Locate every Plasmodium ovale-infected red blood cell.
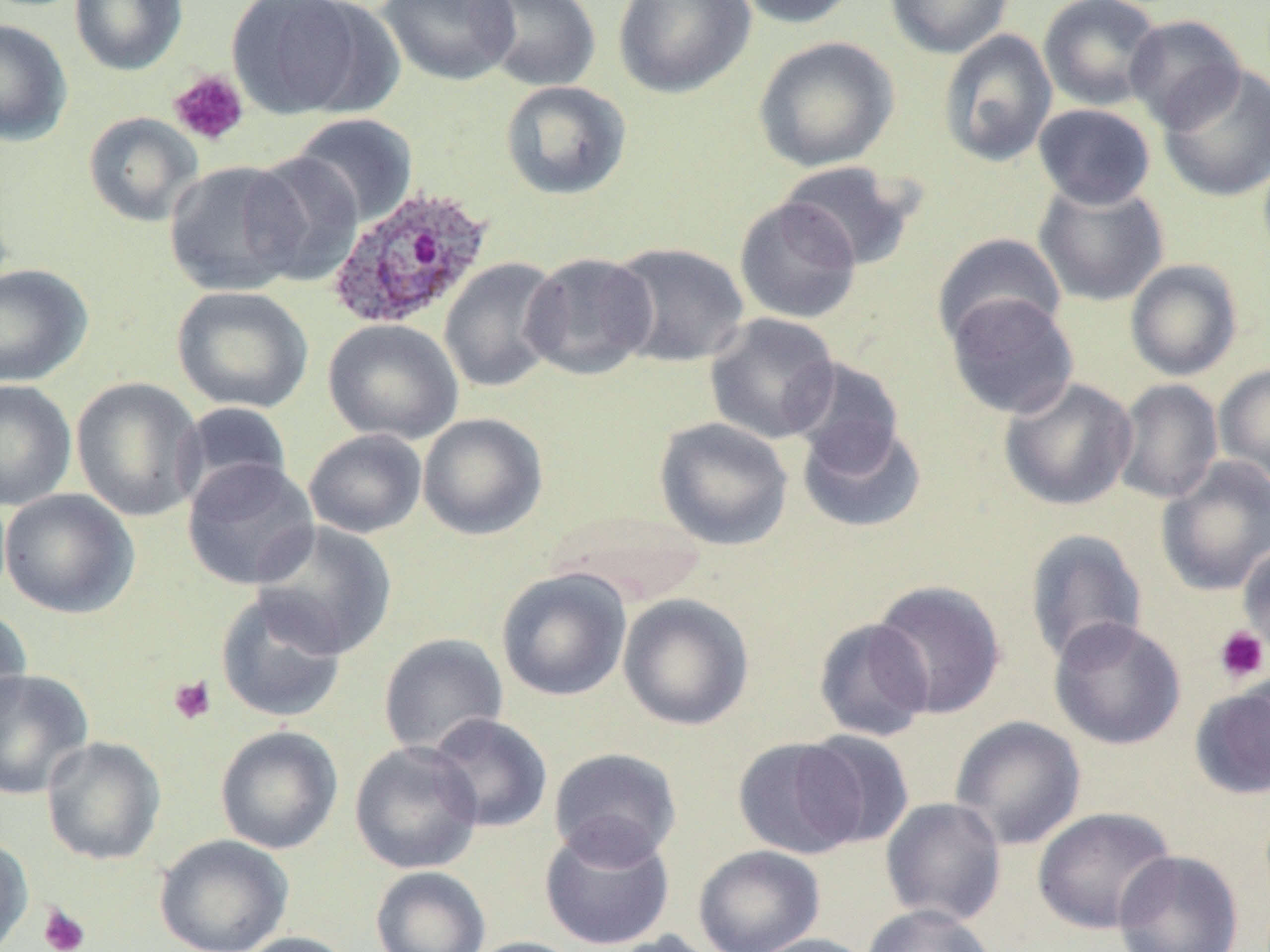
Approximate bounding boxes as (x1,y1)-(x2,y2) corner pairs in pixels.
Plasmodium ovale-infected red blood cells: (326,185)-(493,331).

Summary:
  - Uninfected red blood cell locations: (69,0)-(189,76), (225,0)-(378,119), (377,0)-(519,85), (473,0)-(603,92), (612,0)-(756,99), (731,0)-(862,29), (885,0)-(1014,58), (1038,0)-(1165,111), (1124,14)-(1246,133), (0,18)-(73,146), (937,29)-(1058,168), (752,35)-(900,173), (1157,62)-(1270,202), (500,81)-(632,201), (1033,103)-(1156,209), (82,112)-(203,227), (290,113)-(419,227), (244,152)-(365,286), (163,160)-(308,297), (776,161)-(918,271), (1033,181)-(1169,307), (733,196)-(862,324), (932,232)-(1067,347), (607,241)-(749,368), (521,251)-(658,380), (439,257)-(564,393), (1125,259)-(1243,381), (0,263)-(93,387), (171,285)-(314,414), (945,292)-(1079,419), (704,312)-(841,444), (323,319)-(464,445), (786,357)-(905,473), (1214,363)-(1270,486), (70,377)-(206,521), (998,377)-(1137,511), (0,379)-(77,511), (1113,379)-(1224,505), (173,401)-(294,509), (417,413)-(548,540), (654,417)-(794,550), (797,419)-(928,534), (303,429)-(427,538), (1155,455)-(1270,597), (181,457)-(320,591), (0,488)-(139,618), (547,509)-(708,605), (252,520)-(397,658), (1023,528)-(1149,667), (1237,540)-(1270,660), (495,567)-(632,701), (870,579)-(1007,719), (215,589)-(349,723), (617,593)-(754,730), (0,604)-(32,728), (1048,616)-(1187,750), (813,617)-(933,742), (378,632)-(509,757), (0,668)-(94,800), (1188,678)-(1270,800), (426,712)-(553,834), (949,715)-(1086,850), (215,725)-(344,854), (797,730)-(916,849), (41,737)-(166,865), (733,737)-(867,859), (349,740)-(483,874), (548,747)-(682,866), (880,797)-(1007,926), (1032,806)-(1176,934), (539,820)-(675,951), (0,834)-(33,952), (154,834)-(293,952), (693,845)-(825,952), (1113,849)-(1243,952), (370,865)-(491,952), (861,904)-(997,952), (236,931)-(358,952), (597,931)-(725,952), (744,933)-(879,952), (461,936)-(588,952)
  - Platelet locations: (168,69)-(250,147), (1213,626)-(1269,683), (168,675)-(217,725), (38,903)-(90,952)
  - Slide-level diagnosis: Plasmodium ovale
  - Field of view: one of a larger specimen
  - Magnification: 1000x
  - Preparation: thin blood smear
  - Image size: 1270×952 pixels
  - Modality: optical microscopy
  - Stain: May-Grünwald-Giemsa